Comment on the morphology of the red blood cells.
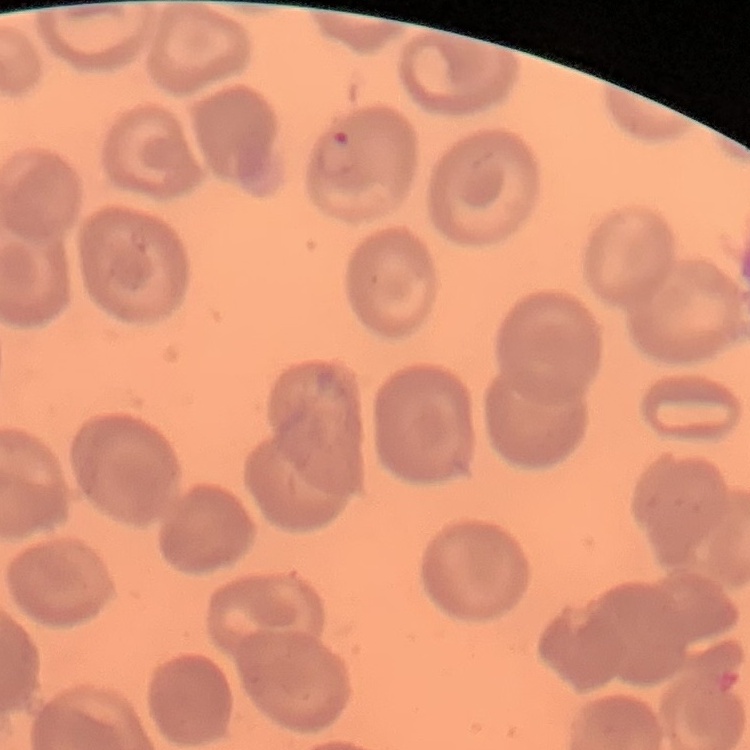

They show no rouleaux formation.

Thin peripheral smear. One tile cut from a larger photomicrograph. Field's or Giemsa stain.